Identify the blood parasite species.
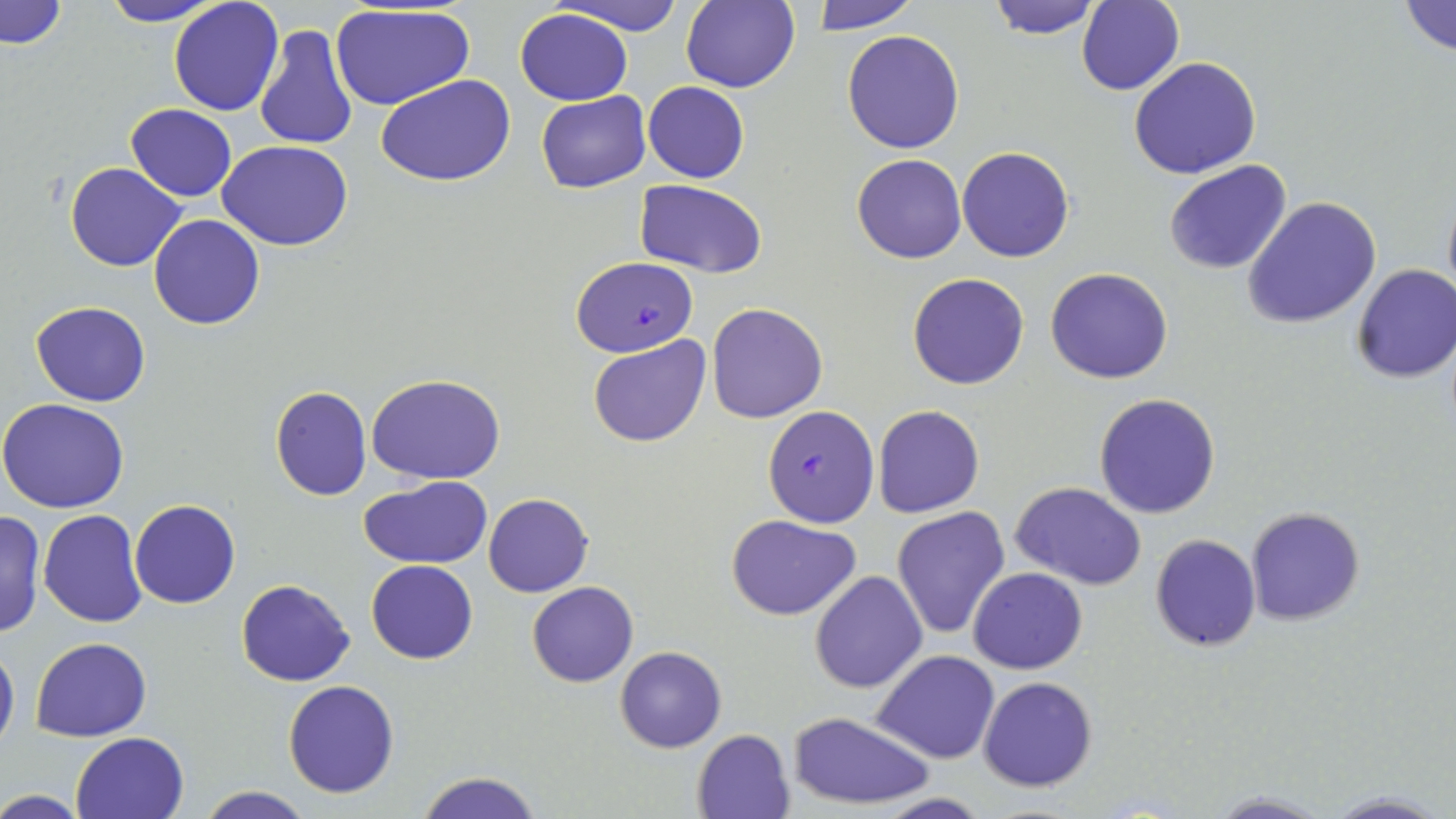

Plasmodium falciparum.

Summary:
  - Coordinate format: approximate bounding boxes as [x1, y1, x2, y2] in pixels
  - Plasmodium falciparum-infected red blood cell locations: [571, 256, 697, 359], [763, 404, 879, 527]
  - Uninfected red blood cell locations: [2, 0, 68, 49], [97, 0, 222, 26], [548, 0, 687, 36], [809, 0, 919, 33], [984, 0, 1105, 39], [169, 1, 284, 117], [680, 1, 799, 93], [1078, 1, 1183, 95], [1397, 1, 1456, 56], [328, 4, 474, 111], [515, 9, 633, 106], [255, 24, 359, 150], [842, 29, 966, 154], [1129, 56, 1262, 179], [376, 75, 518, 186], [643, 81, 749, 183], [536, 92, 651, 192], [126, 103, 237, 200], [218, 139, 352, 250], [956, 146, 1074, 263], [852, 153, 967, 264], [1163, 159, 1293, 274], [65, 162, 186, 271], [635, 180, 767, 277], [1440, 185, 1456, 306], [1242, 196, 1380, 329], [148, 213, 265, 329], [1350, 263, 1456, 384], [1046, 267, 1173, 384], [907, 273, 1030, 390], [32, 301, 150, 407], [707, 302, 828, 423], [588, 335, 712, 448], [366, 373, 505, 484], [271, 385, 372, 501], [1094, 392, 1223, 519], [0, 398, 131, 513], [873, 404, 985, 518], [359, 475, 492, 568], [1011, 482, 1147, 590], [483, 493, 593, 597], [130, 498, 241, 608], [893, 506, 1010, 639], [1245, 506, 1365, 627], [0, 508, 45, 642], [37, 509, 146, 628], [726, 514, 861, 620], [1150, 533, 1262, 650], [366, 559, 477, 664], [969, 567, 1087, 674], [809, 571, 928, 694], [236, 578, 355, 686], [527, 581, 639, 687], [31, 636, 152, 742], [0, 641, 19, 757], [615, 646, 726, 752], [871, 649, 1000, 762], [977, 676, 1097, 792], [282, 680, 400, 799], [786, 712, 936, 809], [692, 728, 796, 818], [71, 731, 188, 818], [415, 771, 546, 819], [196, 785, 313, 819], [0, 790, 94, 819], [1203, 790, 1335, 819], [1322, 790, 1448, 819], [876, 793, 993, 819]
  - Preparation: thin blood film
  - Magnification: 1000x
  - Image size: 1456×819 pixels
  - Modality: light microscopy
  - Field of view: one of a larger specimen
  - Stain: May-Grünwald-Giemsa